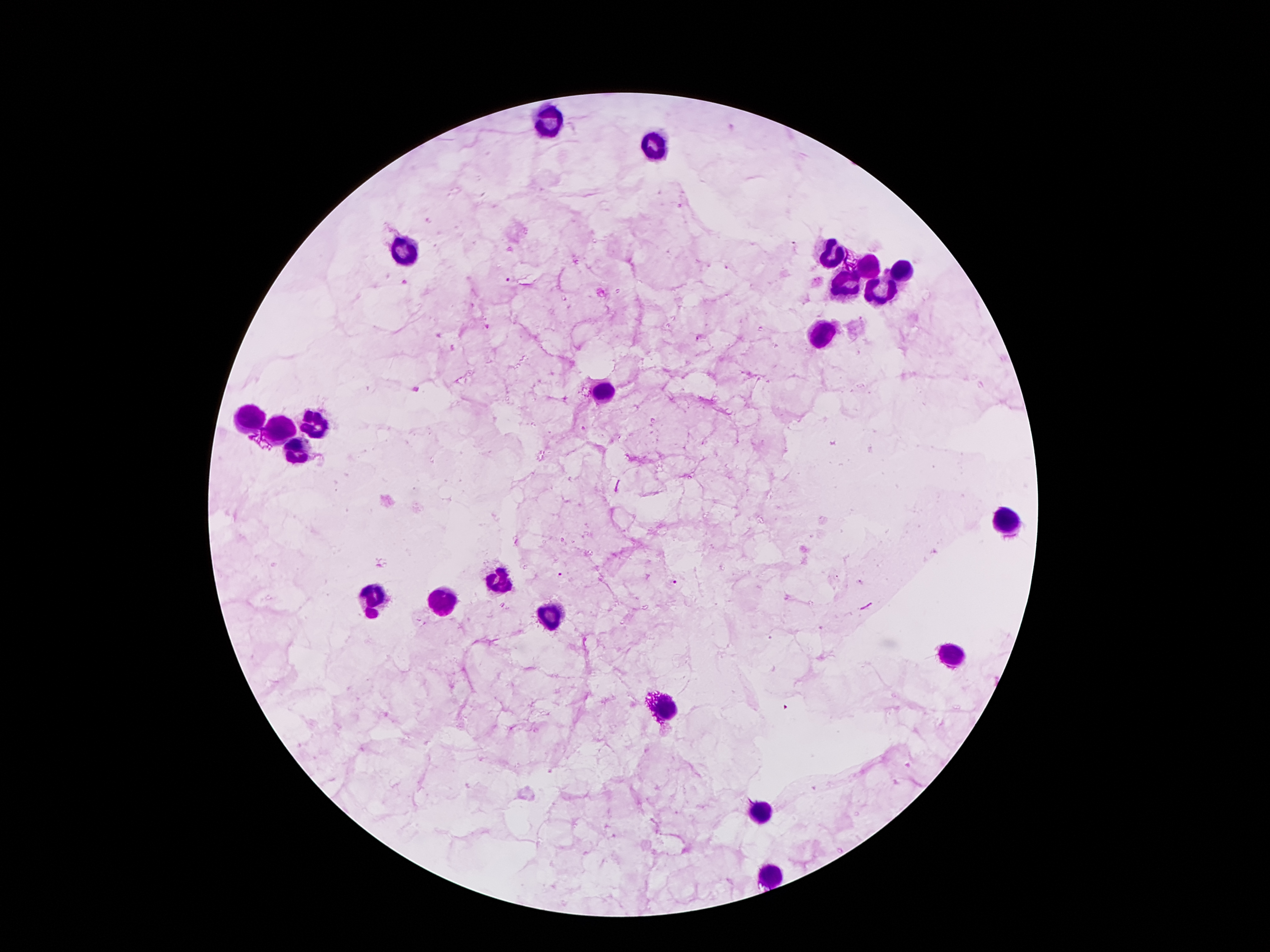 Approximate centers as [x, y] in pixels. Plasmodium parasite locations: [511, 281], [700, 338], [415, 389], [582, 429], [559, 574], [673, 583], [787, 706]. Leukocyte locations: [551, 121], [655, 145], [408, 247], [835, 252], [870, 268], [898, 271], [846, 285], [882, 290], [819, 331], [608, 390], [250, 420], [313, 423], [280, 430], [296, 453], [1010, 521], [499, 579], [376, 593], [441, 602], [550, 614], [952, 654], [665, 712], [760, 814], [770, 877]. Giemsa stain. 100x magnification. Single field of view. Patient malaria status: infected with Plasmodium falciparum. Photographed through the microscope eyepiece with a smartphone camera. Thick blood smear. Image is 1270×952 pixels.